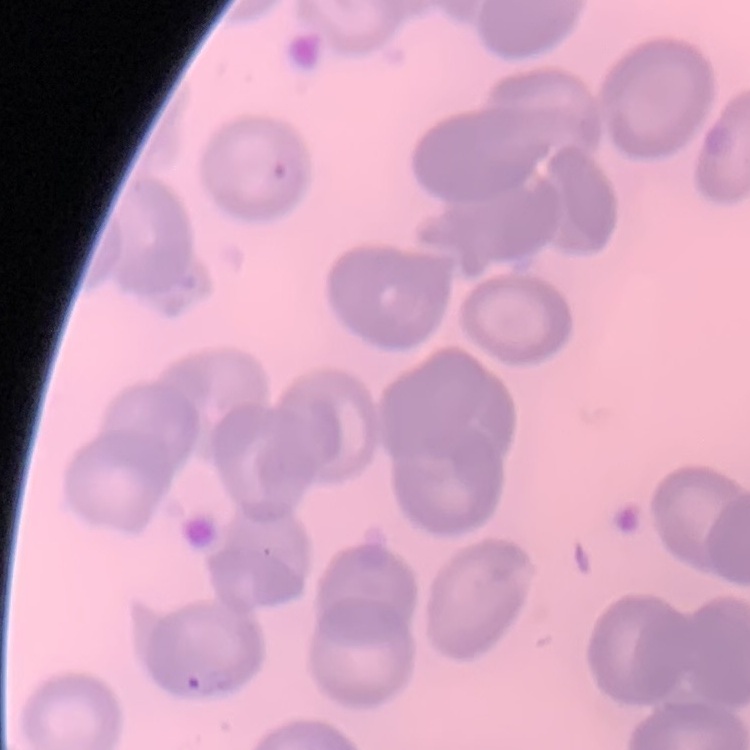

erythrocyte_morphology: no rouleaux formation
image_type: one tile cut from a larger photomicrograph
stain: Field's or Giemsa
preparation: thin blood smear